Give the position of every Plasmodium parasite visible.
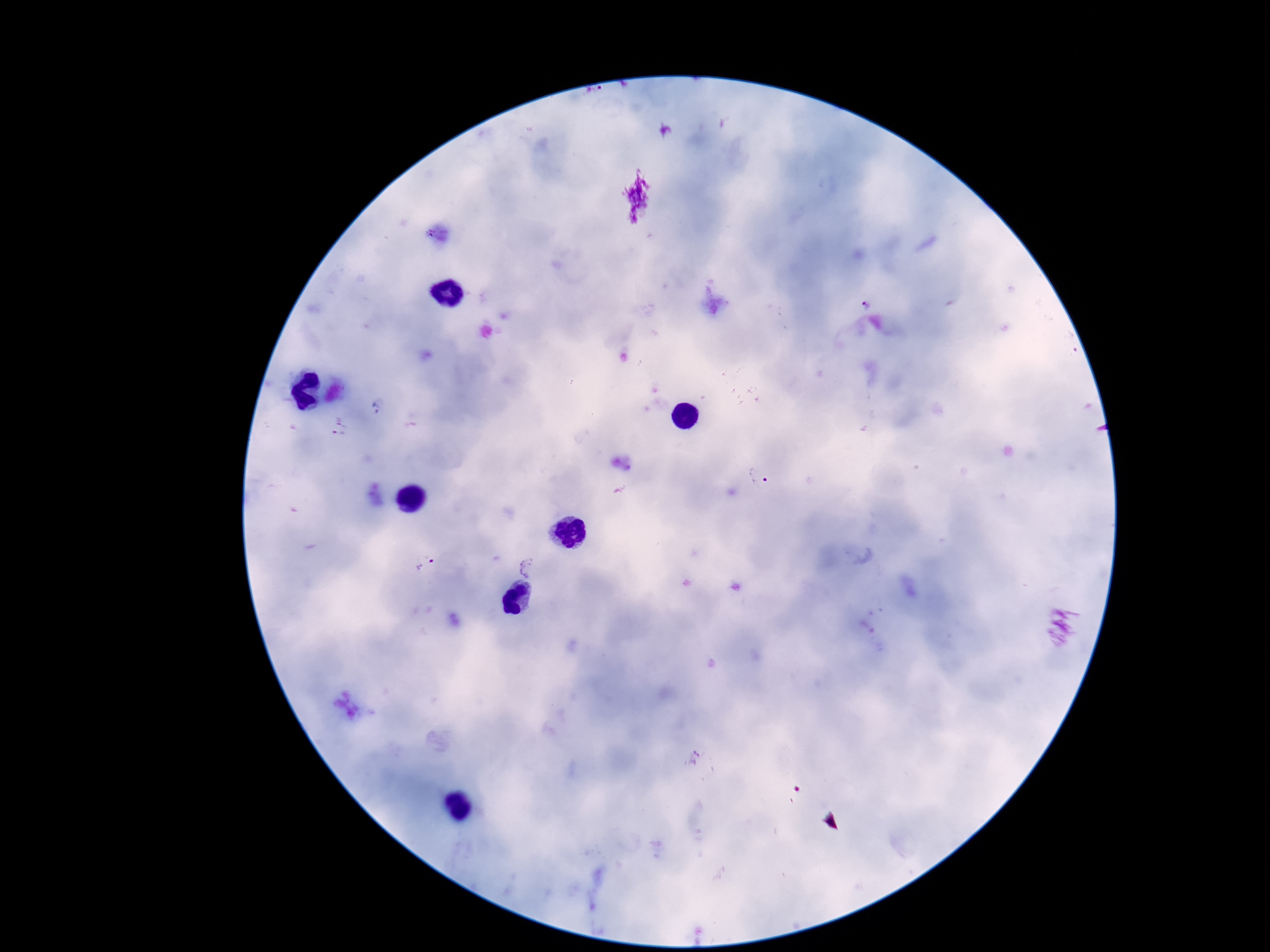
Approximate centers as (x, y) in pixels.
Plasmodium parasites: (340, 429), (759, 475), (425, 565), (529, 567).

Summary:
  - Image size: 1270×952 pixels
  - Patient malaria status: positive
  - Preparation: thick peripheral-blood smear
  - Capture: smartphone camera through the microscope eyepiece
  - Magnification: 100x
  - Field of view: one from this slide
  - Stain: Giemsa